Evaluate for Plasmodium parasites.
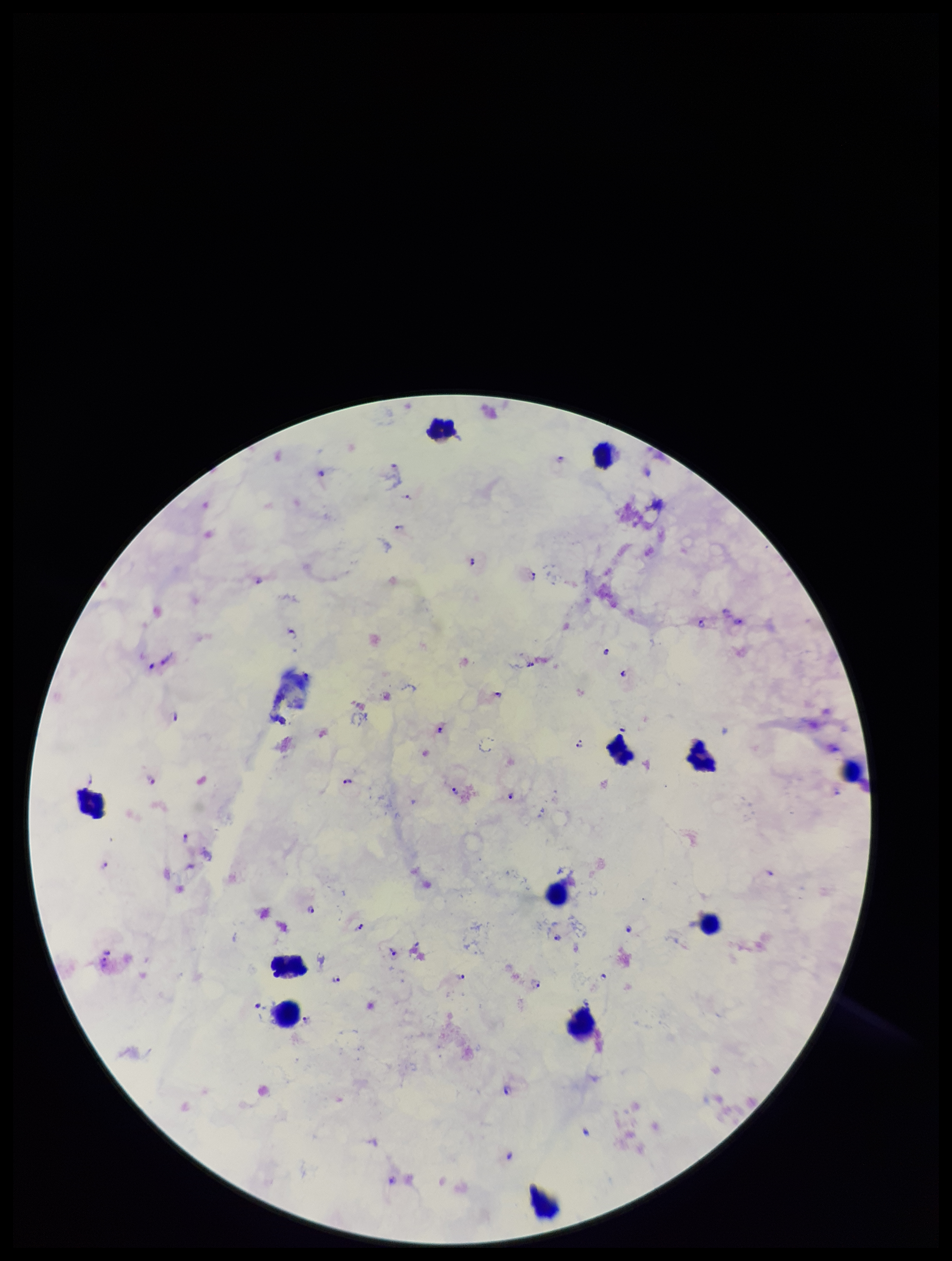
Identified.

Species reported for this patient: Plasmodium falciparum. Image is 952×1261 pixels. One field from this slide. Preparation: thick smear. Giemsa stain. Leukocyte count: 12. Patient malaria status: infected. Parasite count: 29. Smartphone photograph taken through the eyepiece of a microscope.